Outline each uninfected red blood cell.
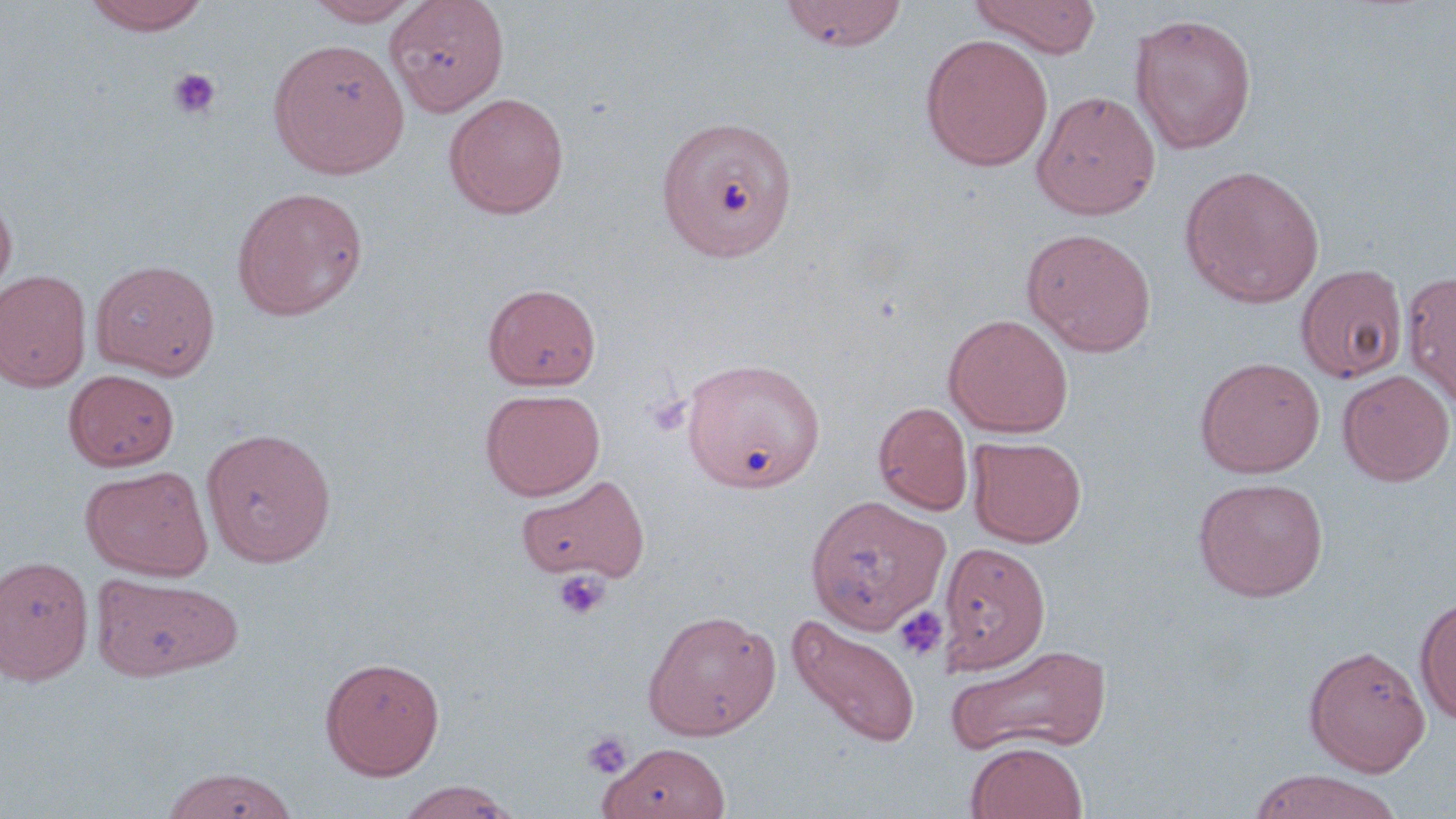
Approximate bounding boxes as named x1/y1/x2/y2 corners in pixels.
Uninfected red blood cells: (x1=81, y1=0, x2=211, y2=35), (x1=302, y1=0, x2=424, y2=26), (x1=384, y1=0, x2=510, y2=116), (x1=780, y1=0, x2=908, y2=51), (x1=968, y1=0, x2=1102, y2=58), (x1=1129, y1=12, x2=1257, y2=155), (x1=919, y1=34, x2=1054, y2=171), (x1=268, y1=39, x2=410, y2=178), (x1=1031, y1=90, x2=1161, y2=220), (x1=443, y1=92, x2=569, y2=219), (x1=658, y1=114, x2=798, y2=262), (x1=1180, y1=164, x2=1325, y2=309), (x1=231, y1=186, x2=369, y2=321), (x1=0, y1=191, x2=17, y2=306), (x1=1022, y1=227, x2=1157, y2=357), (x1=90, y1=259, x2=219, y2=379), (x1=1295, y1=264, x2=1408, y2=383), (x1=0, y1=269, x2=92, y2=392), (x1=1401, y1=270, x2=1456, y2=410), (x1=483, y1=283, x2=601, y2=391), (x1=943, y1=314, x2=1074, y2=437), (x1=681, y1=355, x2=825, y2=492), (x1=1194, y1=356, x2=1325, y2=478), (x1=64, y1=369, x2=180, y2=471), (x1=1337, y1=369, x2=1455, y2=486), (x1=481, y1=388, x2=605, y2=500), (x1=874, y1=401, x2=973, y2=515), (x1=200, y1=426, x2=337, y2=568), (x1=968, y1=436, x2=1087, y2=547), (x1=81, y1=464, x2=214, y2=581), (x1=516, y1=473, x2=651, y2=583), (x1=1193, y1=477, x2=1329, y2=601), (x1=806, y1=494, x2=951, y2=634), (x1=939, y1=540, x2=1050, y2=674), (x1=0, y1=555, x2=94, y2=686), (x1=92, y1=573, x2=242, y2=681), (x1=1415, y1=594, x2=1456, y2=726), (x1=642, y1=609, x2=780, y2=740), (x1=787, y1=614, x2=921, y2=748), (x1=946, y1=643, x2=1113, y2=757), (x1=1303, y1=644, x2=1430, y2=776), (x1=320, y1=656, x2=445, y2=780), (x1=599, y1=742, x2=731, y2=819), (x1=965, y1=742, x2=1088, y2=819), (x1=158, y1=766, x2=299, y2=819), (x1=1246, y1=769, x2=1404, y2=819), (x1=393, y1=781, x2=522, y2=818).

Summary:
  - Platelet locations: (x1=166, y1=68, x2=222, y2=120), (x1=553, y1=570, x2=610, y2=621), (x1=893, y1=605, x2=948, y2=662), (x1=581, y1=730, x2=634, y2=779)
  - Slide-level diagnosis: no evidence of blood parasites
  - Field of view: single
  - Magnification: 1000x
  - Preparation: thin blood film
  - Modality: light microscopy
  - Stain: May-Grünwald-Giemsa
  - Image size: 1456×819 pixels